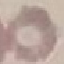
Malaria status: uninfected. Thin smear of blood. Photographed with a smartphone camera at the microscope eyepiece. Giemsa stain. Cell patch, automatically extracted from a larger field of view and resized to 64 × 64 pixels.